Identify the cell.
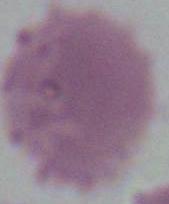

This is an erythrocyte.

Summary:
  - Modality: photomicrograph
  - Magnification: 1000x